State which cell type is depicted.
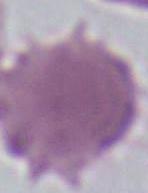
An erythrocyte.

1000x magnification. Micrograph.